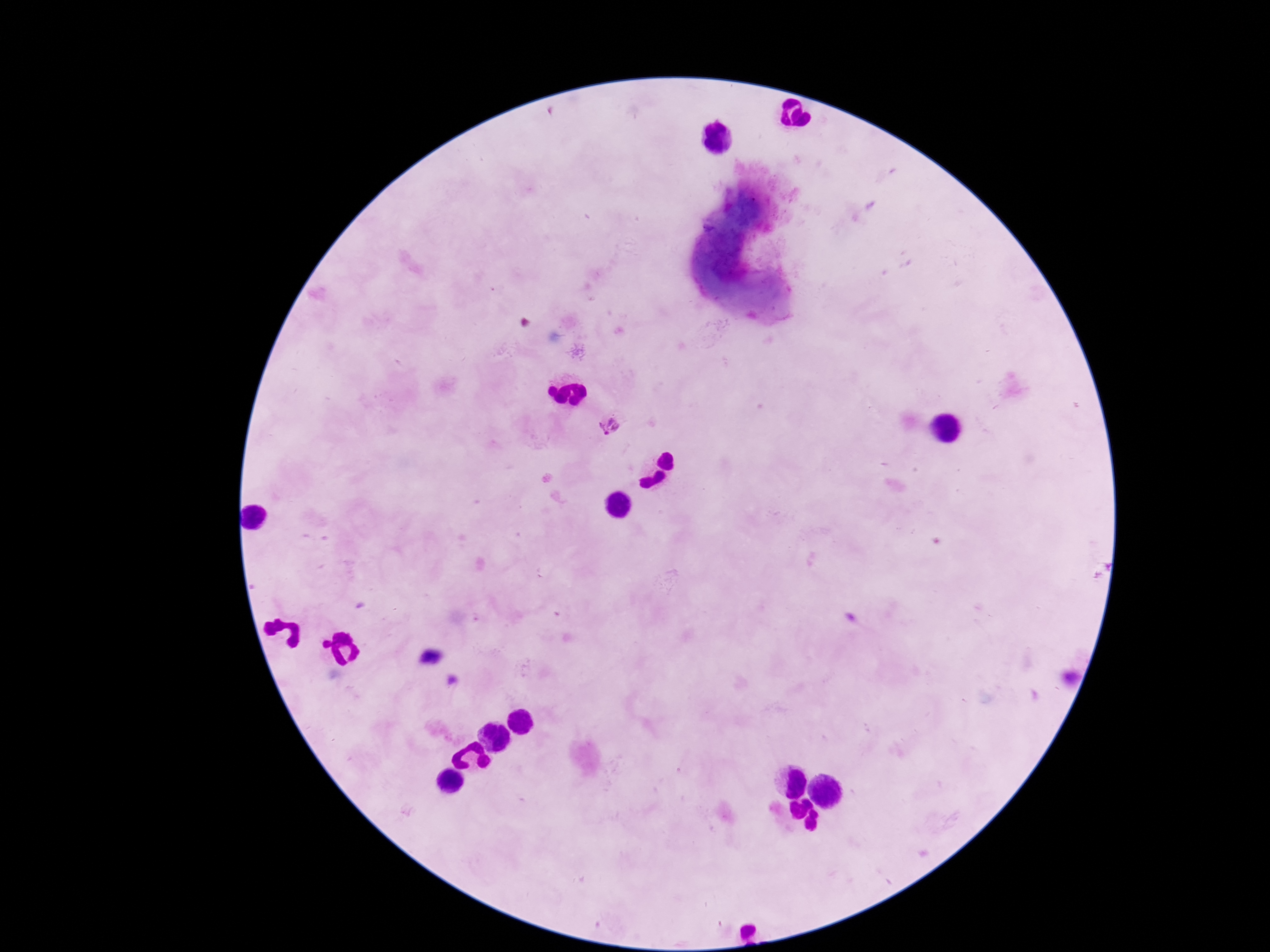

stain = Giemsa
patient malaria status = positive
magnification = 100x
field of view = one from this slide
image size = 1270×952 pixels
capture = smartphone camera through the microscope eyepiece
Plasmodium parasite locations = approximate centers as {x, y} in pixels: {610, 424}
preparation = thick blood smear